Assess this cell for malaria.
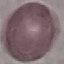

Uninfected.

capture: smartphone through the microscope eyepiece
preparation: thin blood smear
stain: Giemsa
image_type: cell patch, automatically extracted from a larger field of view and resized to 64 × 64 pixels